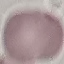 Result: no malaria parasites seen. Thin blood film. Giemsa-stained preparation. Photographed with a smartphone camera at the microscope eyepiece. Automatically extracted cell patch, resized to 64 × 64 pixels.